Assess this cell for malaria.
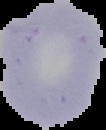
Parasitized.

Summary:
  - Image size: 106×130 pixels
  - Preparation: thin blood smear
  - Image type: cell region segmented out of the field of view; surrounding area masked to black